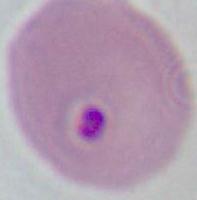

magnification = 400x or 1000x
modality = photomicrograph
identification = Plasmodium